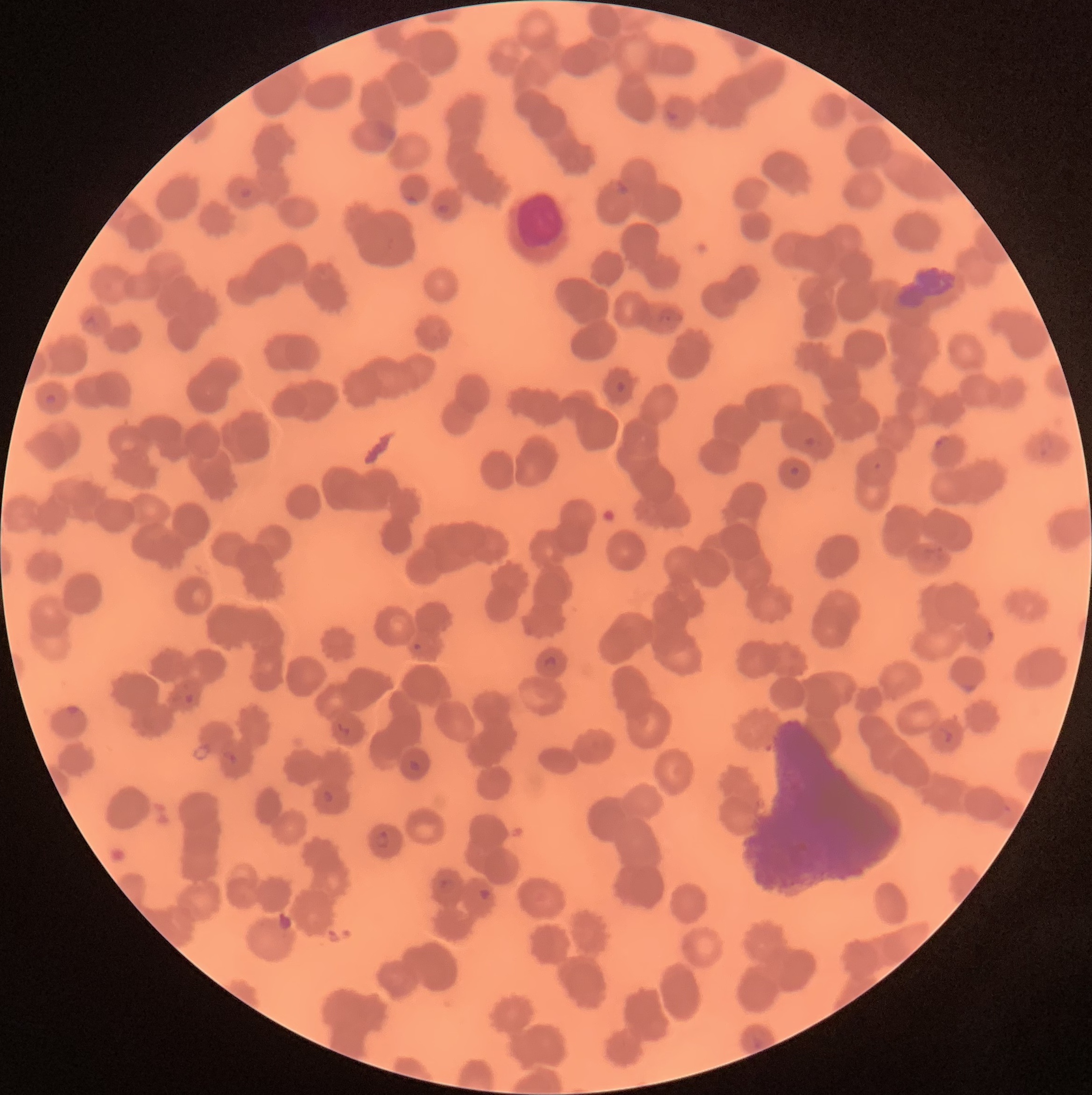

Summary:
  - Coordinate format: approximate bounding boxes as [x1, y1, x2, y2] in pixels
  - Plasmodium parasite locations: [664, 108, 679, 123], [375, 121, 396, 140], [614, 181, 629, 197], [238, 187, 253, 200], [406, 194, 420, 207], [437, 204, 450, 216], [659, 306, 682, 325], [84, 316, 98, 335], [614, 380, 627, 395], [45, 392, 57, 405], [1037, 429, 1054, 459], [802, 434, 817, 448], [934, 435, 950, 450], [872, 461, 883, 471], [789, 466, 801, 477], [923, 546, 949, 565], [986, 628, 996, 646], [412, 643, 423, 652], [541, 655, 557, 671], [962, 681, 976, 694], [183, 692, 194, 705], [65, 705, 81, 717], [337, 722, 351, 736], [939, 727, 952, 745], [224, 750, 238, 767], [408, 758, 420, 772], [322, 789, 334, 805], [374, 829, 390, 850], [439, 878, 456, 898], [477, 886, 493, 901]
  - White blood cell locations: [513, 188, 571, 254]
  - Image size: 1092×1095 pixels
  - Red blood cell morphology: rouleaux formation
  - Preparation: thin blood smear
  - Modality: light microscopy